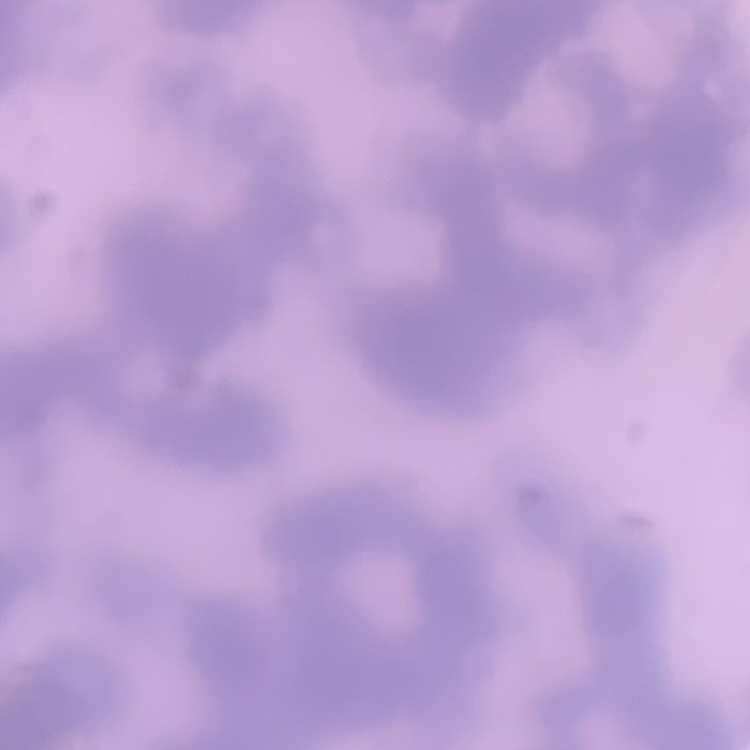
erythrocyte_morphology: rouleaux formation
stain: Field's or Giemsa
preparation: thin blood film
image_type: one tile cut from a larger photomicrograph